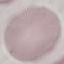

{
  "result": "no malaria parasites detected",
  "capture": "smartphone camera at the microscope eyepiece",
  "image_type": "automatically extracted cell patch, resized to 64 × 64 pixels",
  "stain": "Giemsa",
  "preparation": "thin blood smear"
}